Name the parasite shown.
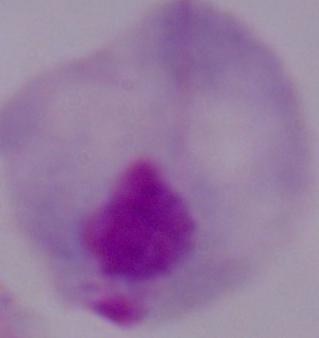
A trichomonad.

Summary:
  - Magnification: 1000x
  - Modality: photomicrograph